Locate and identify every blood parasite.
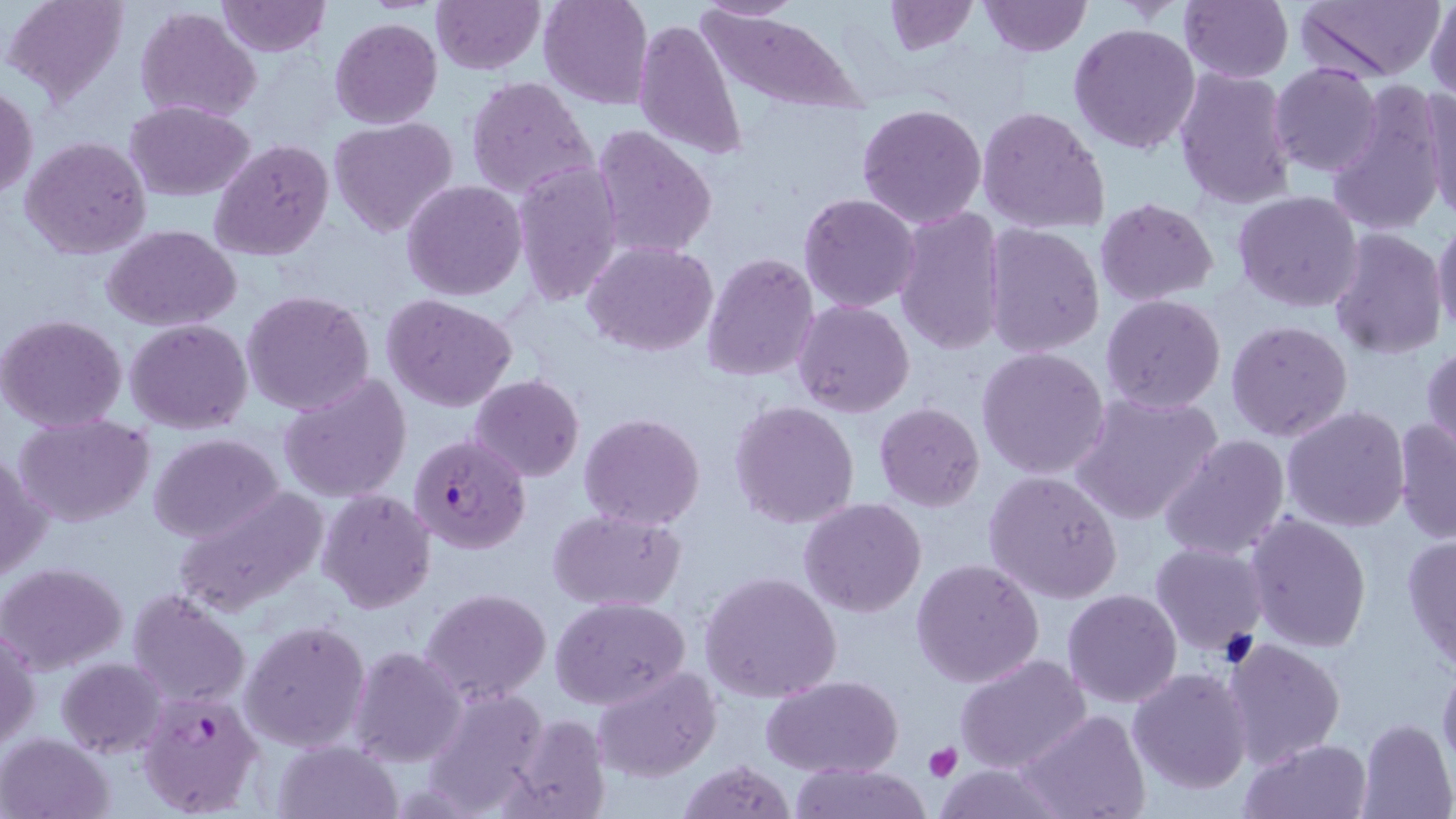

Approximate bounding boxes as (x1, y1, x2, y2) in pixels.
Plasmodium falciparum-infected red blood cells: (408, 432, 530, 556), (138, 688, 264, 817).
No Plasmodium ovale, Plasmodium malariae, Plasmodium vivax, Babesia divergens, or Trypanosoma brucei observed.

Platelet locations: (923, 742, 963, 780). Uninfected red blood cell locations: (4, 0, 132, 108), (214, 0, 331, 56), (430, 0, 544, 75), (538, 0, 654, 110), (881, 0, 977, 54), (977, 0, 1092, 56), (1178, 0, 1293, 83), (1294, 0, 1445, 80), (1426, 0, 1456, 102), (696, 1, 801, 23), (135, 5, 262, 124), (698, 8, 864, 113), (633, 16, 746, 162), (329, 17, 442, 130), (1068, 22, 1204, 156), (1270, 63, 1383, 177), (1172, 66, 1298, 211), (464, 76, 598, 201), (1419, 80, 1456, 222), (1328, 82, 1447, 238), (1, 84, 37, 201), (125, 101, 257, 200), (856, 102, 987, 230), (976, 105, 1110, 235), (328, 118, 459, 238), (590, 124, 718, 261), (20, 136, 151, 260), (210, 138, 333, 262), (511, 160, 625, 306), (402, 180, 527, 301), (1231, 190, 1364, 313), (798, 192, 922, 314), (1096, 197, 1219, 306), (892, 205, 1009, 356), (1433, 218, 1456, 340), (982, 224, 1105, 357), (103, 225, 242, 330), (1327, 227, 1449, 359), (582, 240, 718, 355), (701, 251, 819, 381), (242, 289, 376, 416), (382, 293, 516, 411), (1101, 294, 1227, 414), (793, 301, 914, 418), (0, 313, 128, 431), (126, 319, 254, 435), (1226, 320, 1354, 442), (1421, 343, 1455, 460), (976, 347, 1110, 481), (280, 372, 411, 502), (470, 374, 585, 482), (1069, 391, 1224, 526), (728, 401, 860, 530), (873, 403, 986, 512), (1281, 405, 1411, 532), (579, 412, 706, 529), (14, 415, 154, 527), (1392, 416, 1455, 544), (149, 433, 283, 543), (1157, 434, 1290, 561), (0, 449, 49, 584), (982, 470, 1123, 604), (170, 488, 329, 618), (315, 489, 436, 612), (800, 499, 927, 619), (547, 507, 688, 611), (1244, 512, 1372, 654), (1402, 533, 1456, 672), (1150, 541, 1268, 658), (911, 558, 1044, 688), (0, 561, 128, 675), (699, 570, 842, 703), (420, 588, 551, 705), (1062, 588, 1183, 709), (127, 589, 250, 706), (550, 596, 691, 710), (240, 620, 370, 753), (1, 623, 40, 753), (1223, 637, 1346, 769), (349, 646, 467, 766), (954, 653, 1093, 775), (57, 657, 168, 758), (1437, 657, 1456, 778), (594, 665, 720, 781), (1128, 667, 1252, 795), (762, 676, 902, 779), (424, 686, 549, 815), (1016, 710, 1151, 819), (504, 713, 611, 819), (1357, 717, 1455, 819), (1, 733, 111, 818), (1240, 737, 1373, 818), (274, 740, 402, 819), (677, 758, 799, 818), (929, 760, 1069, 819), (787, 763, 932, 819). Slide-level diagnosis: Plasmodium falciparum. Optical microscopy. Thin blood film. One field of a larger specimen. Image is 1456×819 pixels. May-Grünwald-Giemsa-stained preparation. 1000x magnification.